Assess this cell for malaria.
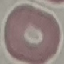

It is uninfected.

Summary:
  - Preparation: thin smear
  - Stain: Giemsa
  - Capture: smartphone camera at the microscope eyepiece
  - Image type: automatically extracted cell patch, resized to 64 × 64 pixels